Outline each blood parasite and name the species.
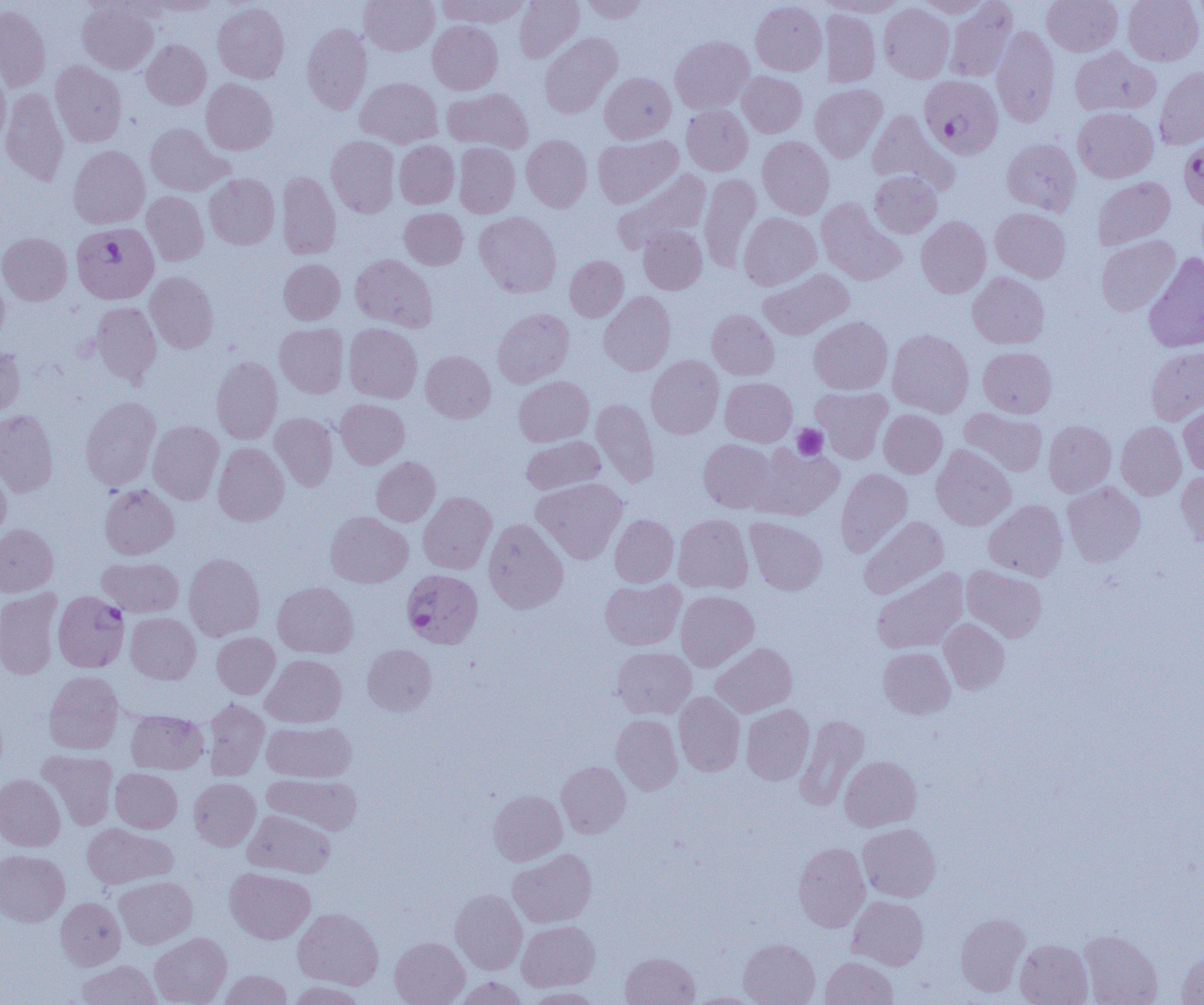

Approximate bounding boxes as [x1, y1, x2, y2] in pixels.
Plasmodium falciparum-infected red blood cells: [919, 74, 1004, 159], [71, 222, 159, 304], [402, 569, 483, 649], [53, 591, 128, 672].
No Plasmodium ovale, Plasmodium malariae, Plasmodium vivax, Babesia divergens, or Trypanosoma brucei observed.

Platelet locations: [793, 424, 828, 459]. Uninfected red blood cell locations: [147, 0, 220, 15], [360, 0, 439, 55], [438, 0, 528, 28], [514, 0, 584, 62], [581, 0, 648, 23], [822, 0, 906, 17], [916, 0, 991, 17], [1042, 0, 1122, 56], [1123, 0, 1204, 66], [77, 1, 159, 74], [751, 1, 827, 75], [944, 1, 1018, 82], [212, 2, 289, 83], [878, 3, 954, 83], [0, 5, 51, 92], [823, 9, 880, 87], [428, 21, 502, 94], [302, 23, 372, 114], [991, 26, 1060, 127], [539, 32, 622, 118], [670, 36, 754, 113], [141, 40, 211, 109], [1070, 46, 1160, 116], [50, 61, 127, 147], [1155, 66, 1204, 150], [0, 69, 10, 148], [737, 71, 807, 137], [600, 73, 676, 144], [355, 77, 442, 148], [201, 78, 278, 154], [810, 84, 887, 162], [0, 88, 69, 186], [443, 88, 533, 153], [681, 105, 753, 175], [1073, 107, 1158, 182], [867, 109, 953, 189], [145, 123, 232, 196], [327, 135, 399, 218], [521, 135, 592, 212], [592, 135, 682, 208], [757, 136, 834, 219], [1179, 136, 1204, 212], [1002, 138, 1081, 216], [394, 140, 459, 209], [454, 143, 520, 218], [68, 146, 149, 228], [613, 169, 712, 252], [277, 171, 341, 259], [870, 171, 942, 237], [204, 173, 279, 249], [699, 175, 762, 273], [1093, 176, 1175, 250], [141, 191, 208, 265], [816, 198, 906, 285], [399, 208, 468, 270], [990, 208, 1071, 282], [474, 212, 561, 297], [739, 212, 821, 290], [917, 216, 991, 298], [638, 226, 707, 294], [0, 232, 72, 305], [1097, 236, 1180, 316], [1143, 253, 1204, 352], [351, 254, 437, 331], [565, 256, 628, 321], [278, 259, 345, 324], [759, 269, 854, 340], [145, 271, 218, 353], [0, 272, 9, 346], [968, 272, 1049, 349], [599, 291, 675, 376], [90, 302, 161, 387], [493, 308, 574, 387], [707, 309, 779, 380], [809, 316, 892, 394], [274, 323, 349, 398], [344, 323, 423, 403], [887, 329, 973, 417], [978, 346, 1056, 417], [1146, 346, 1204, 425], [0, 348, 25, 417], [420, 351, 496, 423], [646, 355, 724, 438], [211, 356, 282, 444], [514, 376, 594, 446], [720, 377, 797, 446], [811, 387, 893, 462], [80, 397, 161, 490], [335, 399, 409, 468], [591, 399, 659, 486], [1178, 402, 1204, 475], [960, 407, 1047, 477], [878, 409, 947, 478], [0, 410, 58, 497], [270, 413, 338, 490], [148, 420, 223, 504], [1043, 420, 1116, 496], [1116, 421, 1186, 500], [522, 436, 605, 494], [699, 439, 778, 513], [213, 442, 288, 526], [752, 445, 843, 520], [931, 445, 1015, 530], [372, 457, 440, 526], [0, 468, 11, 543], [836, 468, 912, 557], [1176, 470, 1204, 547], [531, 478, 627, 564], [1062, 482, 1146, 566], [100, 484, 179, 559], [418, 492, 497, 574], [984, 500, 1067, 580], [325, 511, 413, 588], [610, 514, 679, 587], [673, 514, 753, 593], [859, 516, 948, 599], [745, 517, 828, 595], [484, 518, 568, 613], [0, 524, 58, 596], [184, 553, 265, 640], [97, 557, 184, 616], [962, 565, 1047, 642], [872, 568, 968, 654], [600, 578, 686, 650], [273, 582, 358, 658], [0, 589, 62, 679], [675, 590, 758, 671], [125, 613, 200, 683], [939, 618, 1010, 694], [212, 632, 280, 698], [711, 642, 797, 717], [362, 644, 436, 715], [613, 647, 696, 719], [878, 647, 955, 718], [262, 654, 346, 727], [44, 671, 124, 754], [674, 692, 745, 776], [203, 699, 269, 780], [741, 704, 814, 784], [126, 709, 208, 774], [611, 714, 682, 795], [795, 715, 869, 811], [262, 721, 357, 782], [37, 750, 118, 830], [840, 756, 921, 831], [556, 761, 631, 837], [111, 768, 182, 833], [262, 773, 363, 835], [0, 774, 65, 851], [189, 778, 261, 850], [488, 790, 567, 865], [244, 809, 335, 878], [82, 823, 178, 888], [858, 823, 940, 902], [793, 843, 870, 932], [0, 849, 69, 926], [508, 849, 597, 927], [225, 868, 315, 944], [114, 876, 197, 948], [451, 888, 527, 974], [847, 896, 928, 970], [56, 897, 125, 969], [293, 908, 383, 989], [956, 913, 1030, 996], [517, 920, 599, 991], [1079, 930, 1162, 1005], [149, 932, 231, 1005], [390, 937, 469, 1005], [739, 938, 820, 1005], [1015, 939, 1093, 1005], [1176, 950, 1204, 1004], [620, 951, 700, 1005], [820, 957, 898, 1005], [76, 959, 162, 1005], [218, 970, 292, 1005], [453, 976, 528, 1005], [287, 981, 367, 1005], [525, 987, 602, 1004], [686, 992, 766, 1005]. Slide-level diagnosis: Plasmodium falciparum. 1000x magnification. Optical microscopy. Image is 1204×1005 pixels. One field of a larger specimen. Thin blood smear.